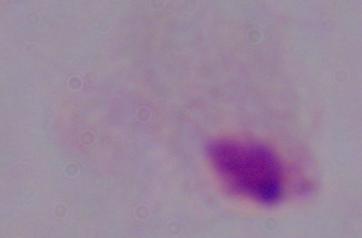

A trichomonad is seen. Micrograph. Captured at 1000x magnification.